Report the malaria status of this cell.
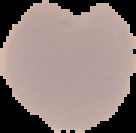
Uninfected.

From a thin blood film. Image is 136×133 pixels. Segmented cell region on a black background.